Describe the morphology of the erythrocytes.
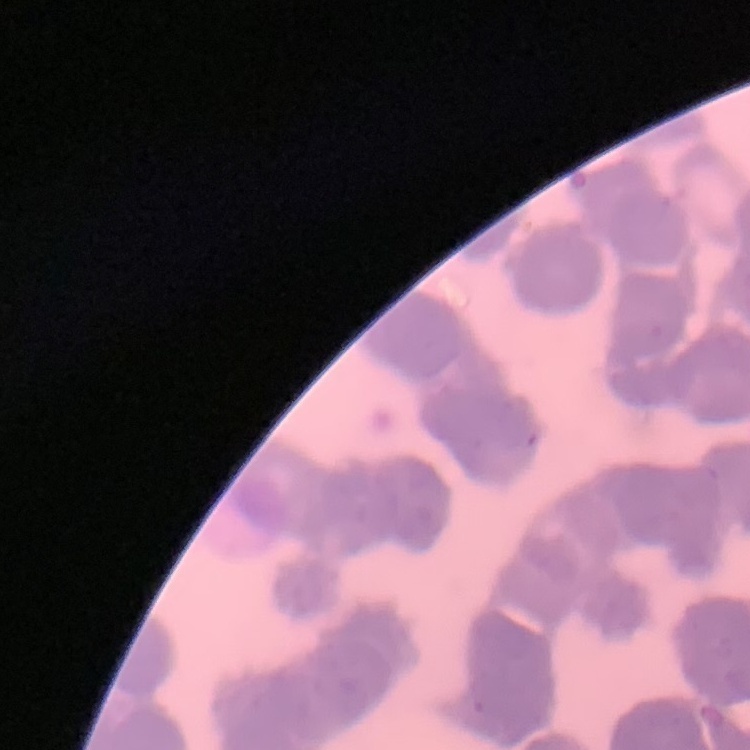

They show rouleaux formation.

image_type: square crop of a larger photomicrograph
preparation: thin blood film
stain: Field's or Giemsa